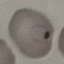

Summary:
  - Malaria status: parasitized
  - Image type: cell patch, automatically extracted from a larger field of view and resized to 64 × 64 pixels
  - Stain: Giemsa
  - Capture: smartphone through the microscope eyepiece
  - Preparation: thin smear